Comment on the morphology of the erythrocytes.
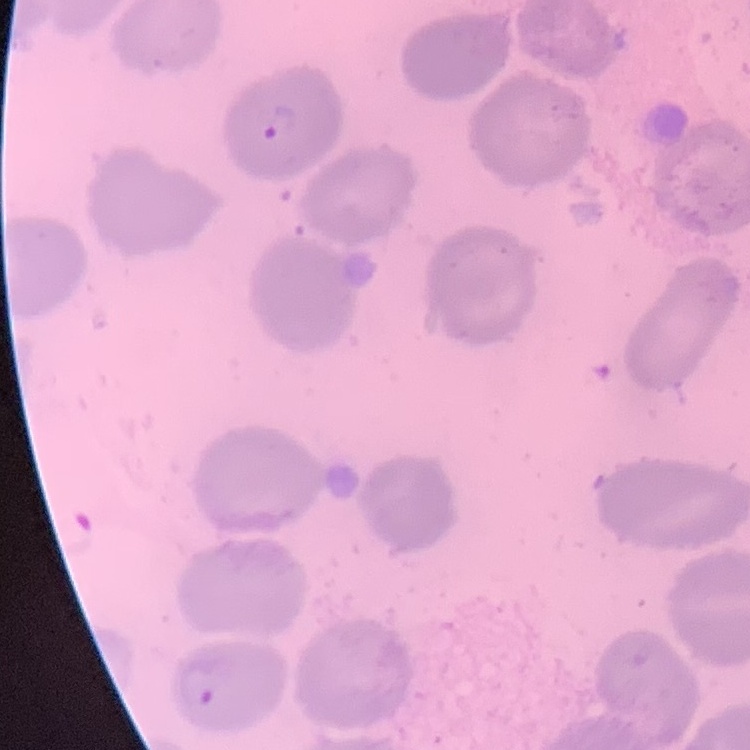
No rouleaux formation.

stain = Field's or Giemsa
preparation = thin peripheral smear
image type = square crop of a larger photomicrograph